Assess this cell for malaria.
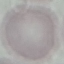
It is uninfected.

Thin blood smear. Cell patch, automatically extracted from a larger field of view and resized to 64 × 64 pixels. Photographed with a smartphone camera at the microscope eyepiece. Giemsa stain.